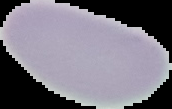
{
  "image_size": "172×109 pixels",
  "preparation": "thin blood film",
  "result": "no Plasmodium parasites detected",
  "image_type": "segmented cell region with the area outside set to black"
}